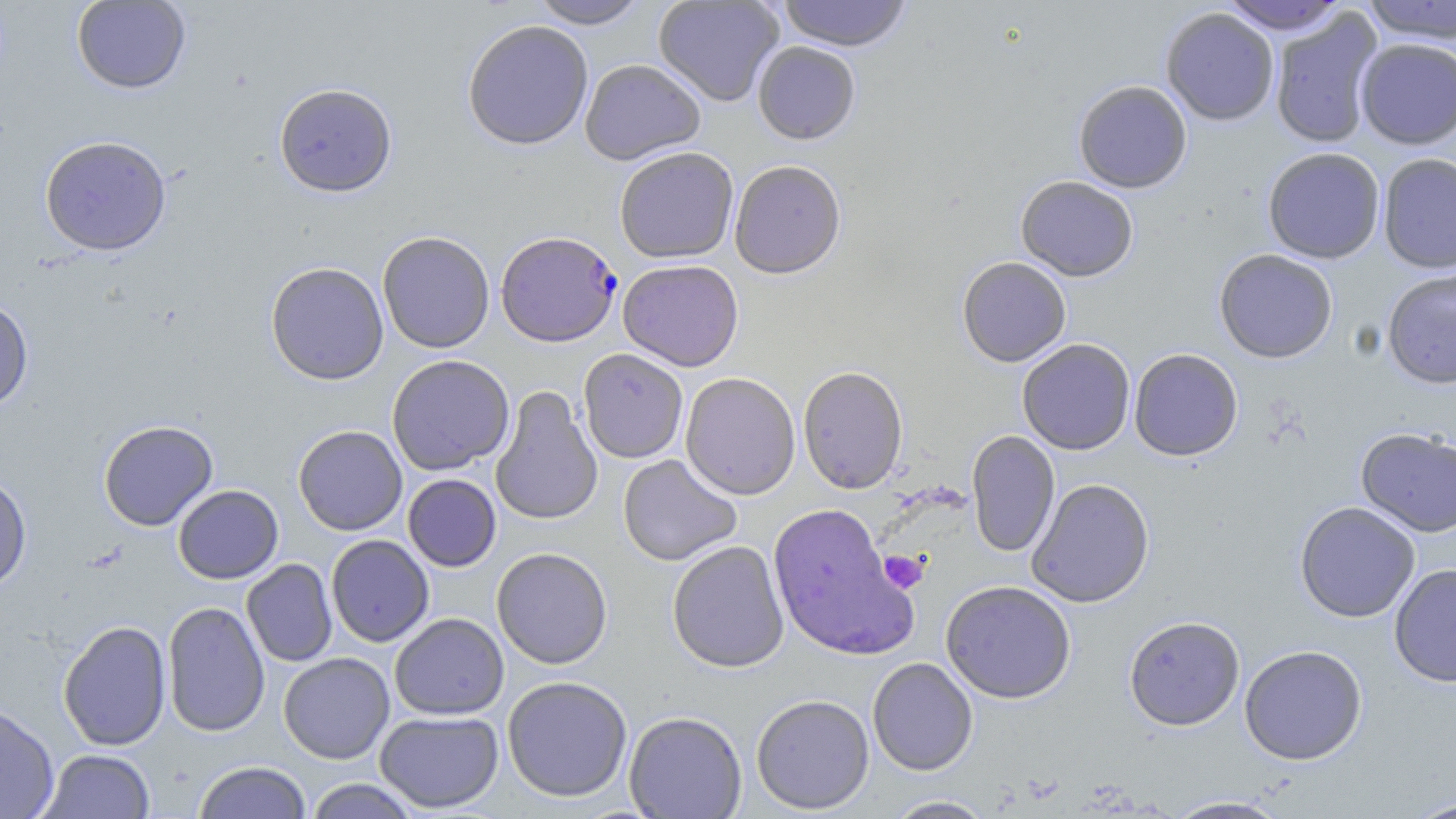
Summary:
  - Coordinate format: approximate bounding boxes as [x1, y1, x2, y2] in pixels
  - Plasmodium falciparum-infected red blood cell locations: [496, 230, 621, 347]
  - Platelet locations: [878, 550, 928, 594]
  - Uninfected red blood cell locations: [528, 0, 650, 29], [653, 0, 785, 107], [776, 0, 912, 52], [1218, 0, 1349, 34], [71, 1, 191, 94], [1359, 1, 1456, 43], [1160, 7, 1279, 126], [1269, 9, 1383, 150], [462, 20, 594, 150], [1355, 38, 1456, 149], [753, 41, 860, 144], [579, 58, 706, 164], [1073, 80, 1192, 194], [273, 82, 397, 196], [39, 135, 172, 256], [614, 146, 739, 263], [1263, 147, 1385, 264], [1377, 153, 1456, 274], [729, 159, 847, 278], [1016, 176, 1138, 281], [377, 231, 495, 353], [1214, 249, 1338, 363], [957, 257, 1071, 367], [618, 259, 744, 371], [265, 261, 389, 385], [1382, 267, 1456, 389], [0, 296, 34, 412], [1017, 338, 1135, 455], [578, 348, 688, 463], [1129, 348, 1243, 461], [387, 354, 514, 475], [797, 366, 909, 494], [680, 372, 801, 500], [490, 385, 603, 525], [98, 420, 218, 531], [293, 425, 407, 535], [1356, 428, 1456, 537], [966, 430, 1060, 558], [617, 454, 742, 566], [0, 474, 32, 595], [402, 474, 501, 572], [1026, 478, 1155, 608], [173, 484, 283, 584], [1294, 501, 1420, 623], [767, 503, 918, 661], [326, 534, 434, 647], [667, 540, 789, 673], [491, 547, 613, 669], [241, 559, 338, 667], [1389, 563, 1456, 687], [940, 580, 1076, 703], [161, 602, 270, 737], [389, 613, 509, 720], [1124, 615, 1245, 731], [57, 620, 171, 751], [1239, 645, 1368, 765], [278, 652, 395, 764], [867, 658, 978, 775], [502, 675, 633, 802], [751, 694, 875, 814], [0, 702, 59, 819], [375, 711, 504, 813], [624, 711, 747, 818], [39, 749, 155, 819], [192, 761, 311, 819], [304, 778, 422, 818], [882, 795, 997, 818], [1163, 796, 1293, 818], [1404, 798, 1456, 819]
  - Slide-level diagnosis: Plasmodium falciparum
  - Stain: May-Grünwald-Giemsa
  - Magnification: 1000x
  - Modality: optical microscopy
  - Field of view: one of a larger specimen
  - Image size: 1456×819 pixels
  - Preparation: thin blood smear